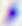

Summary:
  - Modality: micrograph
  - Identification: Toxoplasma gondii
  - Magnification: 400x